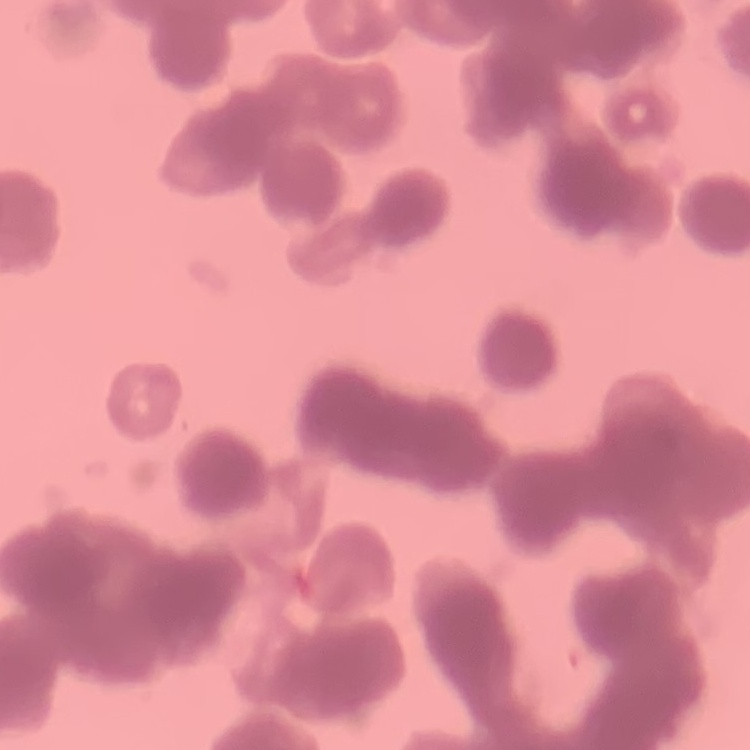

{
  "erythrocyte_morphology": "rouleaux formation",
  "preparation": "thin blood film",
  "stain": "Field's or Giemsa",
  "image_type": "square crop of a larger photomicrograph"
}